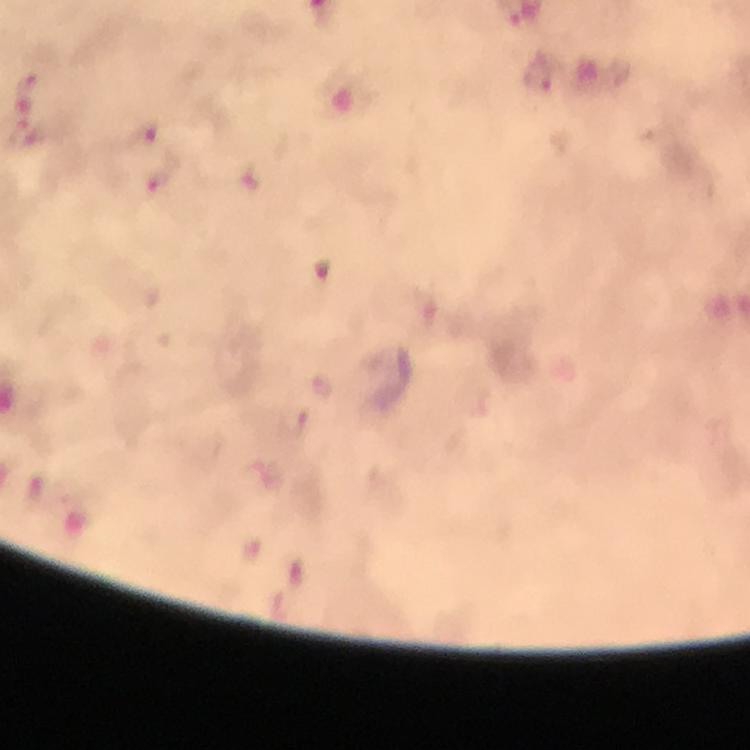
Approximate object centers, in pixels from the top-left corner. Plasmodium parasite locations: (x=536, y=73), (x=145, y=136), (x=251, y=178). Thick blood film. Immersion oil applied. Giemsa stain. 100x magnification. From a diagnostic examination for malaria. Photographed with a smartphone mounted on the microscope. Cropped region of a single field of view. Image is 750×750 pixels.